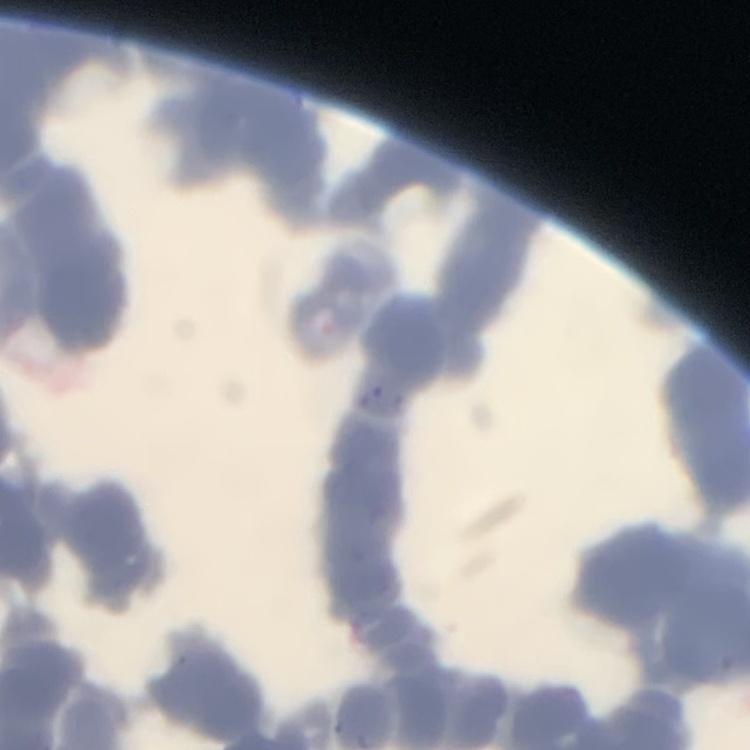
{
  "red_blood_cell_morphology": "rouleaux formation",
  "preparation": "thin blood smear",
  "stain": "Field's or Giemsa",
  "image_type": "one tile cut from a larger photomicrograph"
}